Give the extent of all Plasmodium falciparum-infected red blood cells.
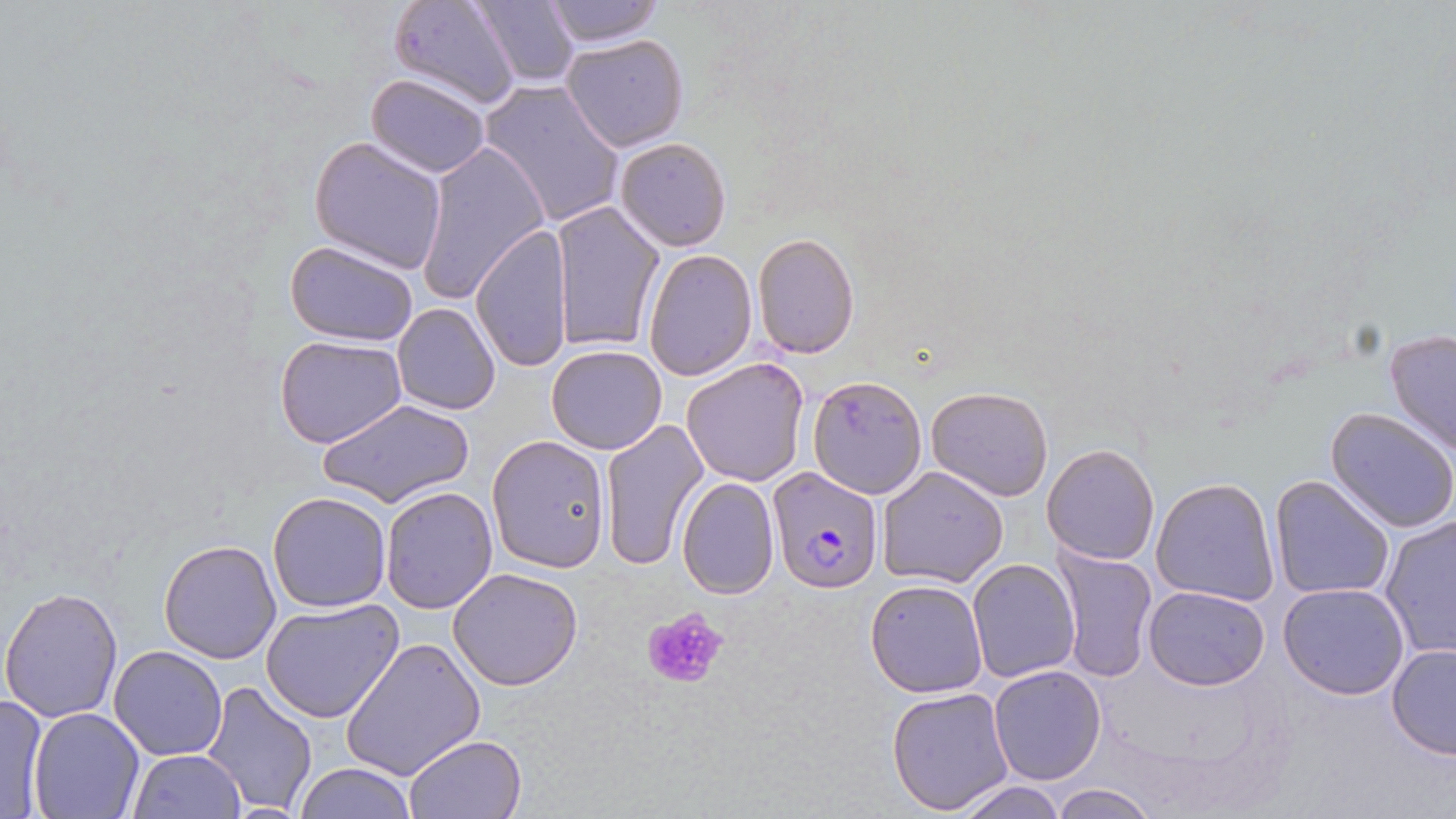
Approximate bounding boxes as [x1, y1, x2, y2] in pixels.
Plasmodium falciparum-infected red blood cells: [766, 467, 885, 593].

slide-level diagnosis = Plasmodium falciparum
preparation = thin blood smear
platelet locations = approximate bounding boxes as [x1, y1, x2, y2] in pixels: [640, 603, 730, 691]
magnification = 1000x
modality = optical microscopy
field of view = one of a larger specimen
stain = May-Grünwald-Giemsa
uninfected red blood cell locations = approximate bounding boxes as [x1, y1, x2, y2] in pixels: [388, 0, 521, 109], [468, 0, 581, 88], [538, 0, 666, 48], [560, 34, 690, 152], [366, 73, 491, 177], [478, 80, 626, 228], [308, 136, 449, 273], [614, 136, 732, 250], [417, 141, 549, 302], [550, 202, 664, 354], [469, 224, 571, 373], [752, 233, 861, 358], [283, 240, 421, 347], [642, 249, 756, 379], [391, 303, 499, 416], [1384, 327, 1456, 458], [275, 334, 405, 449], [546, 344, 668, 455], [681, 356, 811, 487], [807, 372, 928, 499], [927, 386, 1054, 499], [316, 396, 473, 509], [1324, 406, 1456, 534], [598, 416, 709, 570], [487, 434, 611, 572], [1041, 444, 1160, 565], [877, 465, 1009, 587], [1268, 475, 1396, 602], [676, 476, 781, 599], [1150, 477, 1280, 607], [380, 485, 498, 613], [267, 491, 392, 612], [1379, 515, 1456, 659], [158, 538, 280, 663], [1052, 548, 1158, 684], [967, 558, 1082, 683], [448, 567, 583, 691], [864, 577, 989, 698], [1277, 583, 1410, 700], [1142, 584, 1271, 691], [1, 585, 124, 723], [262, 598, 404, 722], [341, 637, 486, 780], [1386, 643, 1456, 760], [110, 645, 227, 760], [988, 664, 1107, 785], [201, 680, 319, 816], [886, 686, 1015, 815], [0, 692, 50, 816], [27, 707, 144, 819], [403, 734, 527, 819], [127, 749, 247, 818], [292, 762, 418, 819], [953, 778, 1067, 819], [1047, 782, 1160, 818]
image size = 1456×819 pixels